Locate and identify every blood parasite.
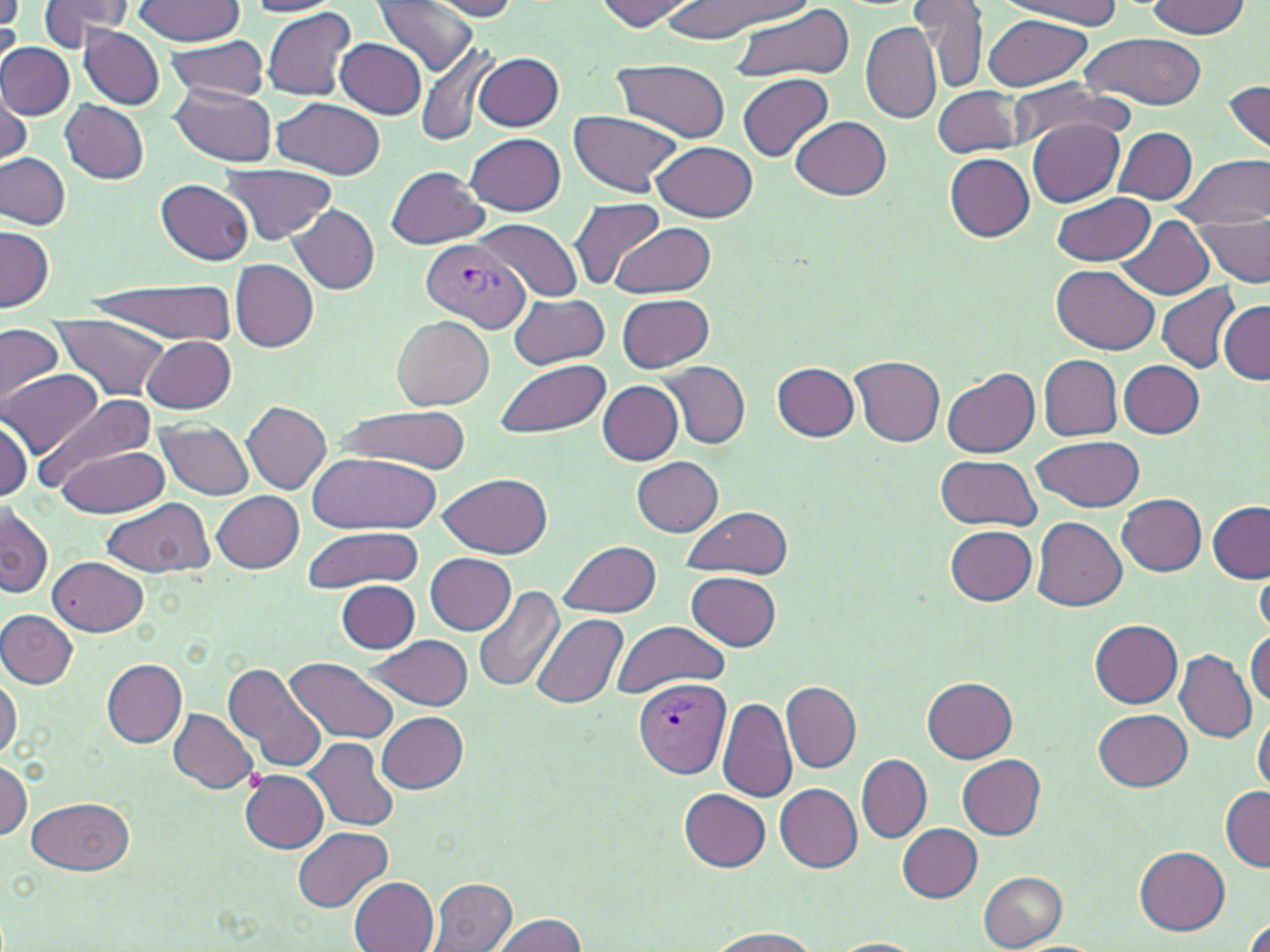
Approximate bounding boxes as (x1,y1)-(x2,y2) corner pairs in pixels.
Plasmodium vivax-infected red blood cells: (421,239)-(528,332), (634,677)-(732,780).
No Plasmodium falciparum, Plasmodium ovale, Plasmodium malariae, Babesia divergens, or Trypanosoma brucei observed.

Summary:
  - Uninfected red blood cell locations: (36,0)-(134,50), (137,0)-(244,45), (245,0)-(344,16), (374,0)-(480,78), (595,0)-(695,29), (993,0)-(1125,24), (1145,0)-(1250,39), (427,1)-(523,20), (661,2)-(808,37), (912,2)-(987,90), (731,4)-(856,83), (260,6)-(357,101), (0,7)-(22,64), (983,15)-(1090,91), (861,20)-(941,124), (79,26)-(164,110), (1080,33)-(1208,110), (164,37)-(272,102), (336,38)-(428,118), (416,41)-(500,147), (0,44)-(73,119), (474,52)-(564,131), (612,60)-(732,143), (738,73)-(833,161), (1007,79)-(1131,148), (1223,79)-(1270,158), (170,86)-(278,165), (933,87)-(1027,158), (0,93)-(31,171), (273,97)-(384,179), (60,98)-(149,183), (569,110)-(684,197), (790,117)-(892,201), (1029,118)-(1125,206), (1113,127)-(1198,204), (466,133)-(566,216), (654,141)-(758,223), (1173,152)-(1268,233), (0,153)-(71,230), (945,153)-(1035,242), (219,163)-(336,246), (387,166)-(489,247), (156,179)-(255,265), (1053,192)-(1155,265), (569,196)-(665,289), (288,204)-(380,294), (1193,205)-(1270,290), (473,218)-(582,303), (1121,218)-(1214,298), (613,221)-(716,298), (1,225)-(53,311), (231,260)-(318,352), (1052,266)-(1159,354), (90,279)-(239,342), (1156,283)-(1243,374), (618,293)-(714,372), (510,294)-(607,370), (1218,299)-(1269,384), (393,314)-(494,410), (45,316)-(173,402), (0,325)-(64,407), (142,335)-(236,414), (1040,355)-(1122,441), (850,356)-(946,447), (494,358)-(610,440), (659,360)-(750,449), (773,361)-(859,442), (1120,361)-(1204,438), (942,368)-(1039,458), (3,370)-(101,459), (598,380)-(684,465), (38,392)-(155,488), (242,400)-(331,494), (336,407)-(467,473), (0,417)-(34,501), (155,419)-(255,500), (1031,434)-(1144,513), (54,447)-(168,515), (307,453)-(445,533), (934,454)-(1042,532), (632,457)-(724,536), (439,472)-(552,558), (213,490)-(304,574), (1118,494)-(1208,575), (102,499)-(214,577), (1,502)-(51,599), (1207,503)-(1269,583), (680,505)-(794,579), (1032,516)-(1127,611), (300,525)-(421,594), (945,525)-(1037,605), (560,540)-(660,617), (425,553)-(515,635), (48,555)-(149,637), (1255,564)-(1270,635), (687,572)-(783,650), (338,581)-(419,652), (474,585)-(565,696), (0,610)-(76,687), (530,613)-(629,709), (610,620)-(730,699), (1090,620)-(1183,708), (1246,632)-(1270,707), (365,635)-(474,711), (1174,649)-(1256,741), (287,657)-(401,745), (102,659)-(187,748), (224,662)-(328,773), (0,673)-(22,760), (922,675)-(1018,763), (782,682)-(861,772), (716,695)-(798,803), (169,709)-(258,794), (1253,709)-(1270,796), (1092,710)-(1194,790), (376,712)-(467,794), (306,737)-(401,834), (857,754)-(931,843), (957,755)-(1046,840), (0,760)-(32,842), (241,770)-(328,854), (774,783)-(861,871), (1220,786)-(1269,872), (680,789)-(771,872), (28,797)-(133,875), (899,823)-(982,902), (293,826)-(392,911), (1135,846)-(1230,934), (978,871)-(1066,950), (349,876)-(438,951), (427,878)-(517,951), (488,914)-(589,952), (1240,915)-(1270,952), (700,924)-(822,951), (828,938)-(927,952)
  - Slide-level diagnosis: Plasmodium vivax
  - Magnification: 1000x
  - Image size: 1270×952 pixels
  - Modality: optical microscopy
  - Preparation: thin blood smear
  - Stain: May-Grünwald-Giemsa
  - Field of view: one of a larger specimen